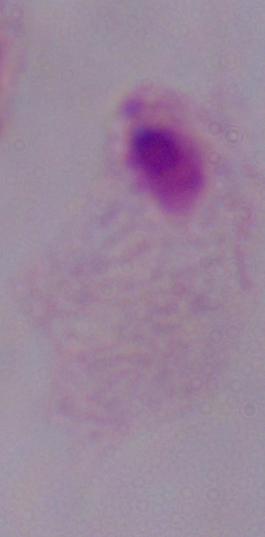

Summary:
  - Modality: photomicrograph
  - Identification: trichomonad
  - Magnification: 1000x